Outline each blood parasite and name the species.
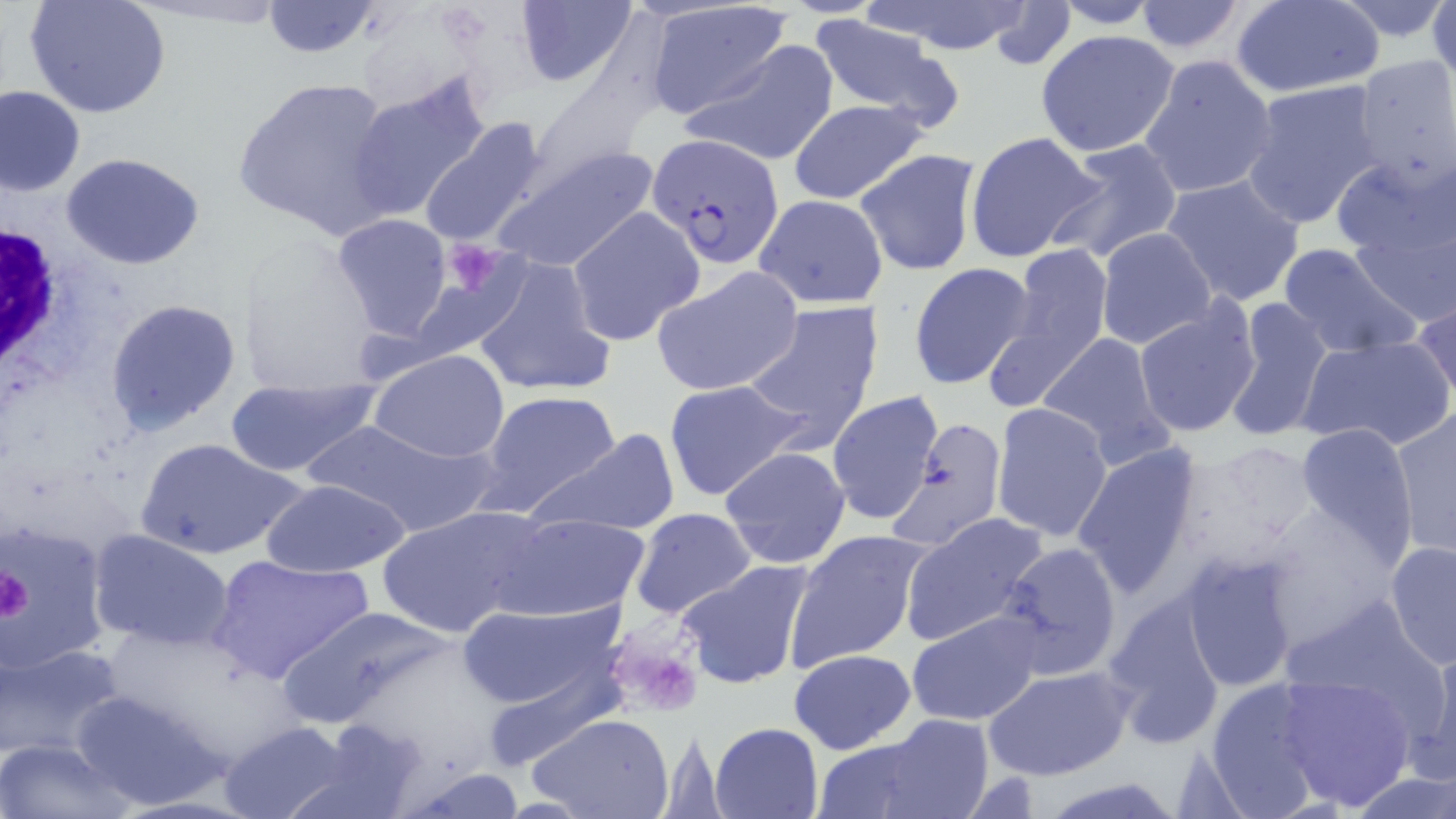

Approximate bounding boxes as (x1,y1)-(x2,y2) corner pairs in pixels.
Plasmodium falciparum-infected red blood cells: (647,137)-(783,270).
No Plasmodium ovale, Plasmodium malariae, Plasmodium vivax, Babesia divergens, or Trypanosoma brucei observed.

Summary:
  - White blood cell locations: (0,205)-(83,393)
  - Uninfected red blood cell locations: (26,0)-(170,118), (261,0)-(384,57), (514,0)-(638,88), (1129,0)-(1251,56), (1230,0)-(1384,98), (1430,0)-(1456,86), (862,1)-(1040,56), (984,1)-(1079,70), (1050,1)-(1164,29), (1330,1)-(1456,46), (642,4)-(796,119), (807,16)-(963,128), (1034,29)-(1182,158), (678,40)-(838,169), (1137,53)-(1279,200), (1351,55)-(1456,192), (347,72)-(491,224), (233,74)-(403,240), (1240,79)-(1384,228), (0,86)-(86,195), (787,99)-(930,205), (418,117)-(550,248), (964,130)-(1107,262), (1048,138)-(1186,265), (486,145)-(662,276), (855,149)-(981,276), (1333,150)-(1456,309), (61,152)-(206,271), (1161,173)-(1306,308), (752,195)-(889,309), (566,206)-(704,346), (330,214)-(451,341), (1094,228)-(1215,350), (1275,239)-(1424,360), (991,243)-(1115,402), (235,244)-(390,396), (470,255)-(616,399), (907,261)-(1037,390), (652,265)-(804,396), (1410,295)-(1456,403), (106,298)-(241,435), (1222,298)-(1333,444), (1132,299)-(1262,438), (739,300)-(884,447), (1034,332)-(1176,469), (1295,335)-(1453,452), (369,348)-(510,464), (225,378)-(379,477), (662,378)-(811,503), (478,388)-(625,516), (826,391)-(945,526), (991,401)-(1114,543), (1391,408)-(1455,559), (304,417)-(498,536), (1293,421)-(1419,557), (526,427)-(682,536), (135,436)-(301,561), (1071,443)-(1206,598), (719,446)-(851,569), (261,478)-(412,579), (376,505)-(544,637), (630,508)-(758,623), (488,512)-(650,622), (900,513)-(1049,647), (4,519)-(113,673), (89,529)-(234,652), (784,530)-(932,670), (1384,539)-(1456,668), (993,542)-(1124,680), (208,552)-(376,687), (1178,552)-(1309,691), (675,559)-(817,690), (1098,596)-(1227,746), (454,602)-(624,710), (273,604)-(455,730), (906,609)-(1045,727), (0,642)-(127,760), (789,648)-(917,754), (1407,649)-(1456,786), (475,655)-(627,773), (982,664)-(1133,780), (1272,672)-(1415,810), (1199,678)-(1334,817), (70,687)-(229,810), (528,714)-(676,819), (302,717)-(435,819), (815,719)-(994,819), (217,720)-(354,819), (708,722)-(823,818), (0,738)-(133,819), (398,767)-(527,817), (1352,773)-(1456,818), (1038,778)-(1189,818)
  - Platelet locations: (440,237)-(509,298), (0,563)-(33,623), (598,622)-(709,721)
  - Slide-level diagnosis: Plasmodium falciparum
  - Image size: 1456×819 pixels
  - Magnification: 1000x
  - Preparation: thin blood film
  - Modality: optical microscopy
  - Field of view: one of a larger specimen
  - Stain: May-Grünwald-Giemsa